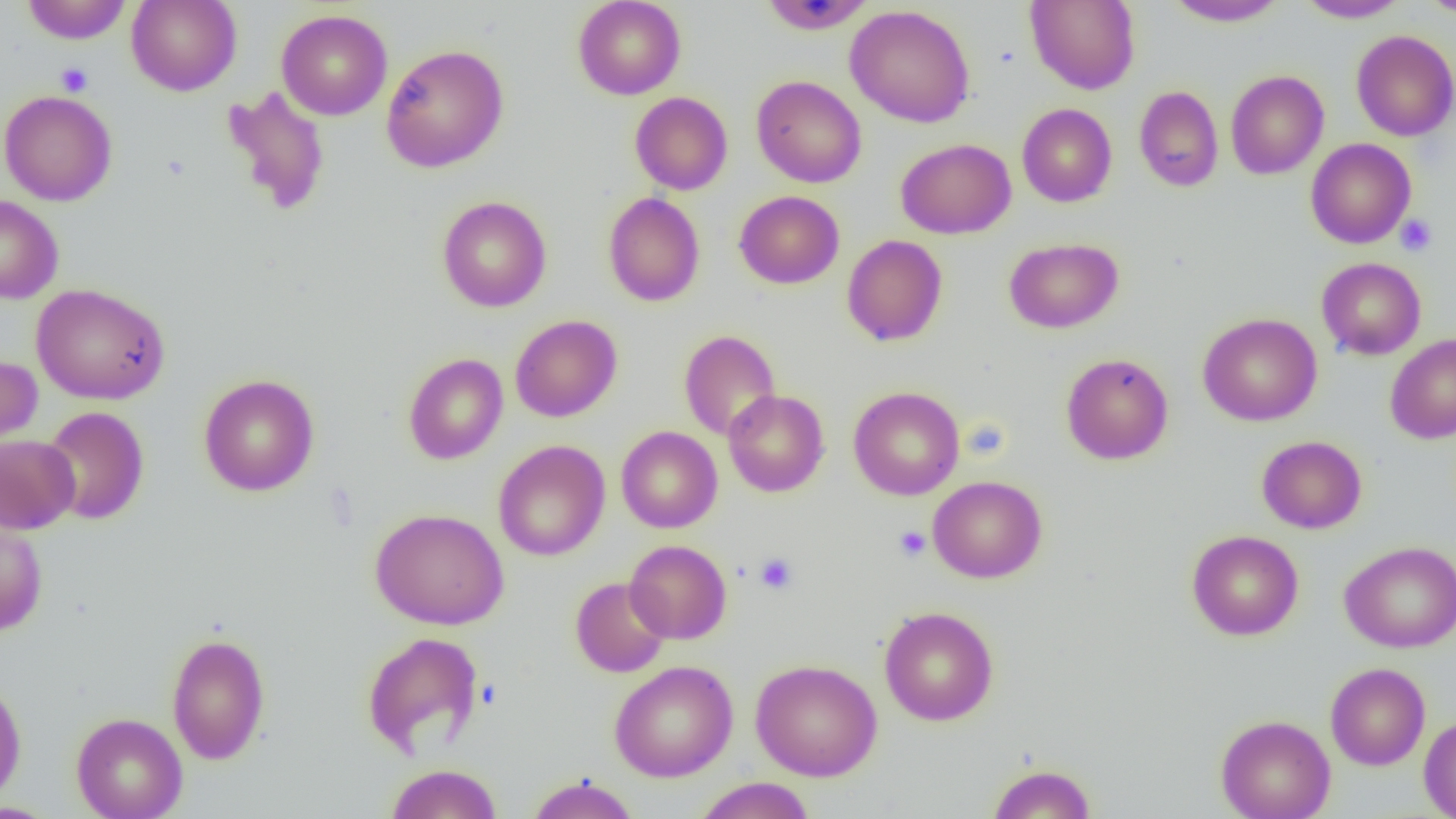 Approximate bounding boxes as (x1,y1)-(x2,y2) corner pairs in pixels. Platelet locations: (55,62)-(93,96), (1395,214)-(1437,257), (894,525)-(931,562), (755,552)-(798,594). Uninfected red blood cell locations: (21,0)-(132,44), (126,0)-(242,96), (572,0)-(687,100), (1025,0)-(1140,94), (1162,0)-(1290,27), (1295,0)-(1410,23), (1418,0)-(1456,16), (758,1)-(877,34), (845,4)-(975,128), (276,9)-(393,120), (1351,30)-(1456,141), (381,44)-(509,173), (1225,70)-(1329,179), (751,75)-(867,188), (1134,85)-(1224,192), (221,86)-(330,217), (0,89)-(117,206), (630,91)-(733,195), (1017,103)-(1117,207), (895,138)-(1016,239), (1305,138)-(1416,248), (734,190)-(844,289), (603,192)-(705,307), (0,195)-(63,304), (436,196)-(552,312), (842,235)-(948,346), (1004,237)-(1123,334), (1316,257)-(1427,360), (30,283)-(170,405), (1197,312)-(1323,426), (510,314)-(622,422), (678,329)-(782,441), (1385,334)-(1456,444), (403,353)-(508,465), (1061,353)-(1173,465), (0,354)-(42,454), (198,374)-(320,496), (849,386)-(964,500), (723,389)-(829,497), (41,406)-(149,525), (616,426)-(723,533), (0,434)-(80,533), (1256,435)-(1367,534), (493,440)-(610,561), (928,476)-(1047,583), (369,508)-(509,630), (0,511)-(48,636), (1187,529)-(1303,641), (625,540)-(732,644), (1339,540)-(1456,653), (570,576)-(671,677), (879,606)-(998,725), (361,631)-(485,759), (166,632)-(271,765), (750,659)-(882,781), (609,660)-(738,782), (1325,662)-(1430,770), (0,677)-(28,808), (71,712)-(188,819), (1215,714)-(1336,819), (1419,715)-(1456,818), (384,763)-(503,819), (987,763)-(1096,818), (525,775)-(640,819), (693,777)-(817,819), (0,802)-(61,818). Slide-level diagnosis: negative for blood parasites. Thin blood smear. Image is 1456×819 pixels. 1000x magnification. Light microscopy. Single field of view.